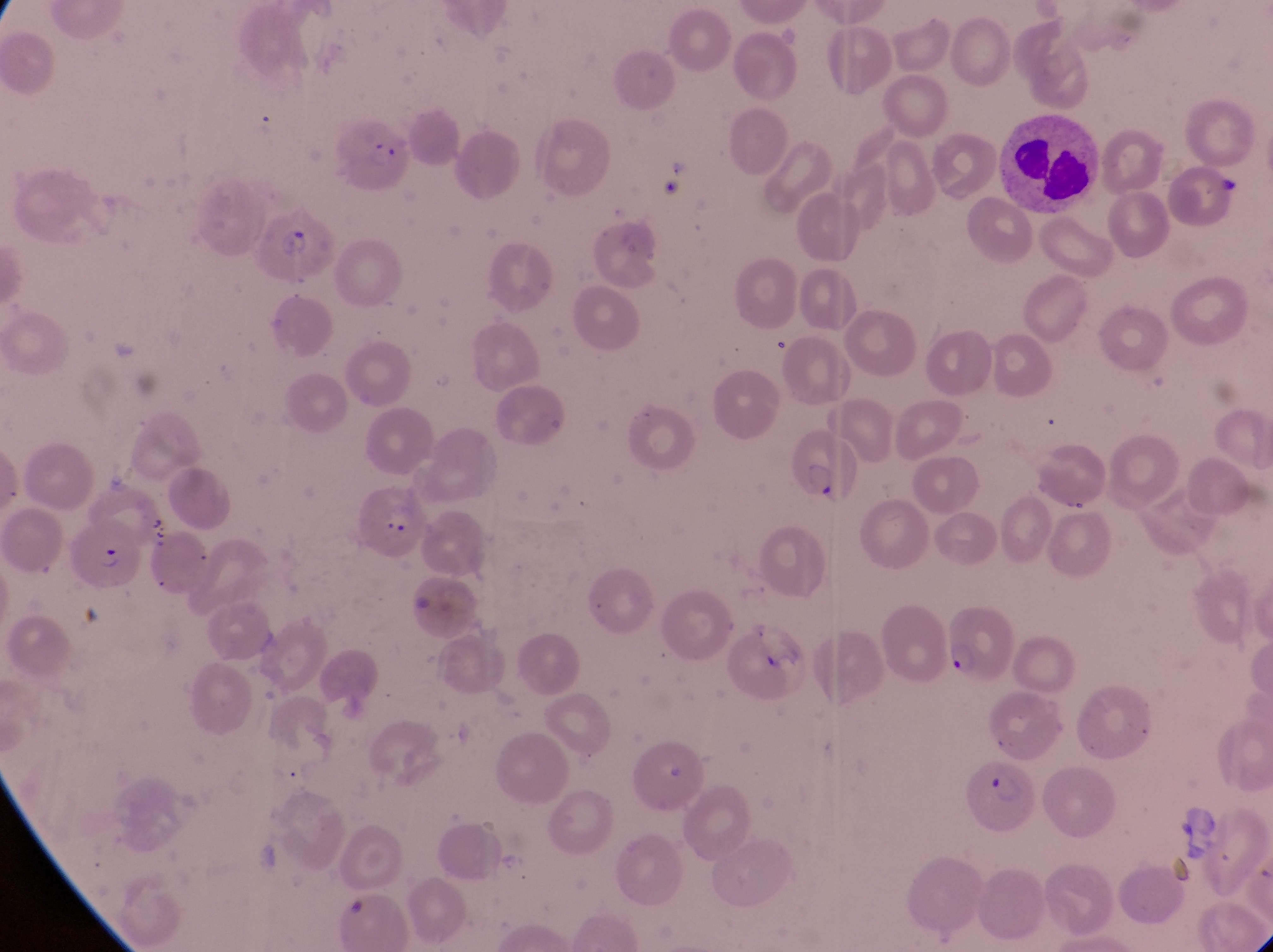
capture = smartphone photograph through the eyepiece of an Olympus CX-23 microscope
image size = 1273×952 pixels
magnification = 1000x
leukocyte locations = approximate bounding boxes as [left, top, right, bottom] in pixels: [1008, 110, 1100, 222]
preparation = thin blood smear
country = Uganda
parasitised red blood cell locations = approximate bounding boxes as [left, top, right, bottom] in pixels: [337, 123, 415, 195], [254, 210, 337, 290], [796, 430, 865, 515], [354, 489, 428, 566], [70, 517, 147, 602], [944, 609, 1013, 689], [959, 759, 1044, 839]
field of view = single